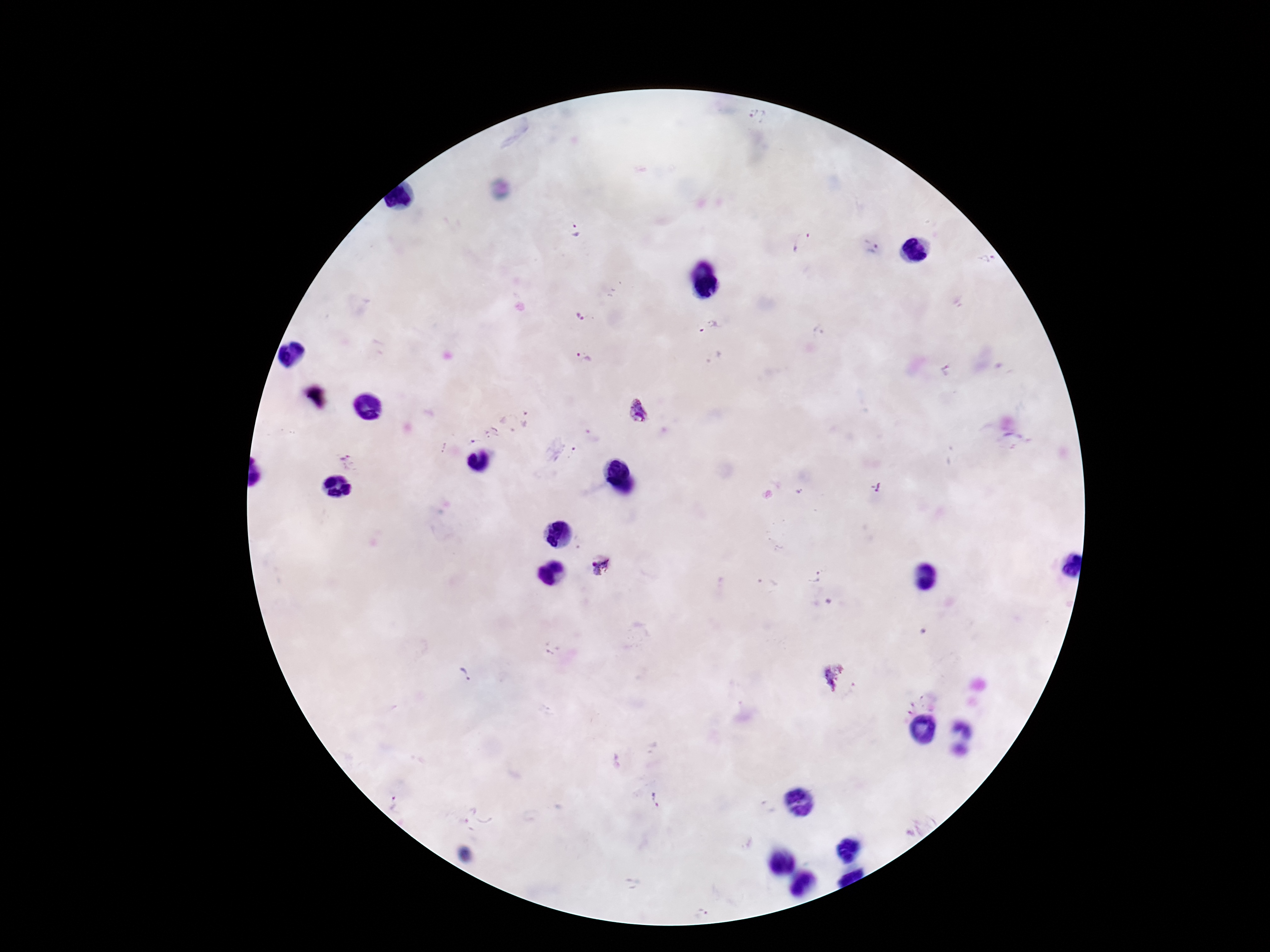

{
  "capture": "smartphone camera through the microscope eyepiece",
  "stain": "Giemsa",
  "magnification": "100x",
  "patient_malaria_status": "infected",
  "plasmodium_parasite_locations": "approximate centers as (x, y) in pixels: (756, 116), (575, 230), (803, 243), (874, 249), (578, 317), (707, 327), (585, 357), (640, 411), (527, 418), (491, 433), (471, 442), (573, 453), (351, 463), (600, 565), (815, 577), (465, 672), (831, 676), (656, 799), (468, 813)",
  "field_of_view": "single",
  "preparation": "thick peripheral-blood smear",
  "image_size": "1270×952 pixels"
}